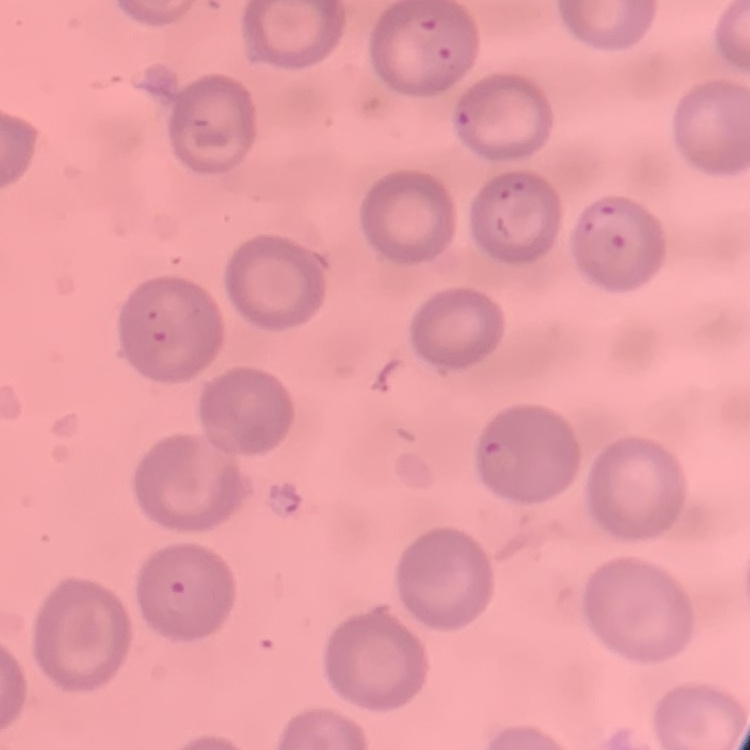 The red blood cells show no rouleaux formation. Thin blood smear. Stained with either Field's or Giemsa. Square crop of a larger photomicrograph.